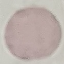
result = no malaria parasites seen
image type = cell patch, automatically extracted from a larger field of view and resized to 64 × 64 pixels
capture = smartphone camera at the microscope eyepiece
stain = Giemsa
preparation = thin blood smear